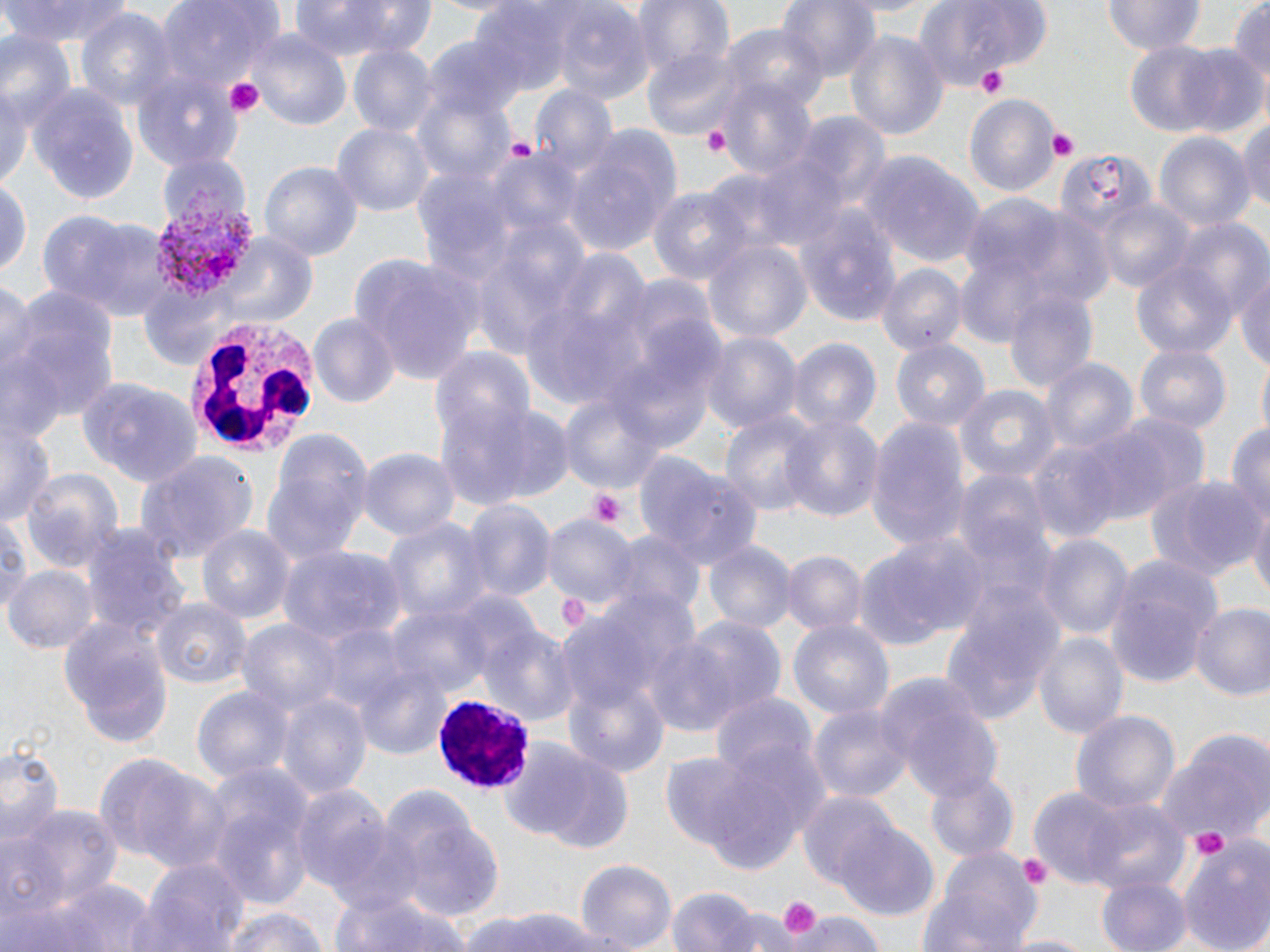

Approximate bounding boxes as (x1, y1, x2, y2) in pixels. White blood cell locations: (187, 321, 317, 461), (432, 693, 536, 792). Platelet locations: (976, 65, 1011, 98), (224, 77, 265, 120), (701, 127, 731, 157), (1048, 129, 1077, 161), (504, 136, 539, 163), (589, 489, 627, 528), (559, 594, 586, 626), (1189, 827, 1234, 864), (1018, 856, 1053, 889), (776, 893, 822, 940). Plasmodium vivax-infected red blood cell locations: (149, 183, 260, 300). Uninfected red blood cell locations: (0, 0, 137, 45), (287, 0, 434, 58), (778, 0, 883, 86), (1105, 0, 1205, 55), (1228, 0, 1270, 88), (158, 1, 279, 90), (632, 1, 735, 80), (919, 2, 1053, 91), (550, 4, 653, 103), (469, 5, 570, 97), (74, 8, 176, 111), (719, 22, 825, 115), (845, 27, 949, 143), (1, 30, 76, 128), (246, 30, 349, 127), (427, 34, 527, 124), (1119, 39, 1240, 139), (1176, 43, 1270, 140), (347, 45, 435, 137), (643, 47, 744, 139), (132, 67, 239, 170), (714, 77, 815, 180), (3, 81, 40, 194), (31, 85, 139, 207), (532, 87, 620, 182), (415, 88, 517, 188), (964, 97, 1058, 194), (799, 111, 889, 210), (1236, 112, 1270, 219), (334, 122, 433, 220), (1152, 130, 1254, 236), (563, 132, 680, 258), (156, 151, 250, 236), (753, 151, 850, 253), (1058, 152, 1152, 233), (862, 153, 983, 268), (258, 160, 363, 262), (0, 178, 30, 282), (647, 184, 753, 287), (962, 194, 1067, 285), (1097, 199, 1194, 294), (36, 206, 165, 321), (797, 207, 902, 327), (1014, 207, 1112, 310), (1170, 219, 1269, 323), (207, 227, 321, 322), (704, 239, 812, 347), (551, 249, 651, 341), (354, 254, 486, 387), (1129, 258, 1238, 363), (876, 262, 968, 357), (1235, 266, 1270, 377), (0, 278, 39, 401), (140, 279, 236, 366), (3, 283, 121, 436), (1005, 288, 1098, 397), (520, 303, 645, 410), (308, 313, 401, 410), (704, 330, 800, 434), (788, 340, 880, 438), (893, 341, 989, 435), (1135, 345, 1230, 437), (430, 346, 533, 453), (1040, 359, 1137, 458), (78, 377, 205, 490), (955, 385, 1060, 487), (557, 388, 670, 499), (441, 402, 575, 510), (721, 408, 819, 521), (781, 411, 884, 526), (1, 413, 57, 526), (1093, 413, 1211, 523), (865, 418, 971, 549), (1224, 418, 1270, 530), (261, 428, 375, 567), (1027, 438, 1124, 544), (358, 447, 459, 545), (135, 449, 256, 565), (639, 456, 762, 568), (21, 470, 121, 575), (956, 471, 1053, 569), (1147, 474, 1263, 581), (459, 499, 556, 607), (1248, 503, 1270, 604), (0, 514, 31, 612), (379, 515, 494, 630), (541, 515, 638, 612), (82, 522, 185, 640), (196, 525, 294, 625), (1036, 531, 1134, 641), (850, 532, 982, 649), (612, 533, 705, 623), (703, 540, 795, 636), (278, 548, 404, 647), (780, 551, 866, 638), (1107, 556, 1223, 688), (6, 565, 99, 656), (938, 578, 1068, 725), (153, 599, 250, 691), (387, 603, 492, 704), (1188, 604, 1270, 700), (58, 614, 175, 750), (237, 616, 346, 719), (651, 617, 784, 733), (789, 618, 894, 722), (480, 626, 580, 730), (1034, 629, 1129, 740), (355, 660, 455, 761), (562, 675, 673, 779), (876, 675, 1002, 803), (192, 684, 293, 786), (276, 688, 372, 800), (707, 690, 817, 786), (810, 701, 911, 805), (1071, 709, 1181, 816), (1157, 730, 1270, 848), (502, 737, 633, 854), (0, 743, 62, 846), (663, 743, 805, 870), (92, 753, 227, 874), (199, 762, 317, 909), (924, 772, 1018, 865), (291, 784, 394, 897), (1029, 786, 1134, 888), (799, 789, 904, 892), (1080, 798, 1191, 898), (9, 803, 124, 907), (398, 817, 504, 923), (324, 818, 429, 920), (836, 822, 940, 919), (1177, 834, 1270, 952), (921, 848, 1044, 952), (138, 857, 250, 952), (576, 860, 677, 950), (1096, 871, 1191, 952), (36, 875, 158, 952), (666, 885, 761, 952), (329, 893, 472, 952), (216, 906, 333, 952), (713, 908, 798, 952), (471, 909, 603, 952), (788, 910, 884, 952), (1003, 931, 1094, 952). Slide-level diagnosis: Plasmodium vivax. May-Grünwald-Giemsa-stained preparation. Thin blood film. Light microscopy. Image is 1270×952 pixels. Captured at 1000x magnification. One field of a larger specimen.